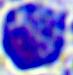
400x magnification. Micrograph. A leukocyte is shown.